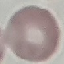
Result: negative for malaria parasites. Thin blood film. Giemsa stain. Automatically extracted cell patch, resized to 64 × 64 pixels. Acquired by smartphone through the microscope eyepiece.